Classify this cell by malaria status.
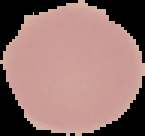
Uninfected.

Summary:
  - Image size: 145×136 pixels
  - Image type: cell region segmented out of the field of view; surrounding area masked to black
  - Preparation: thin blood film